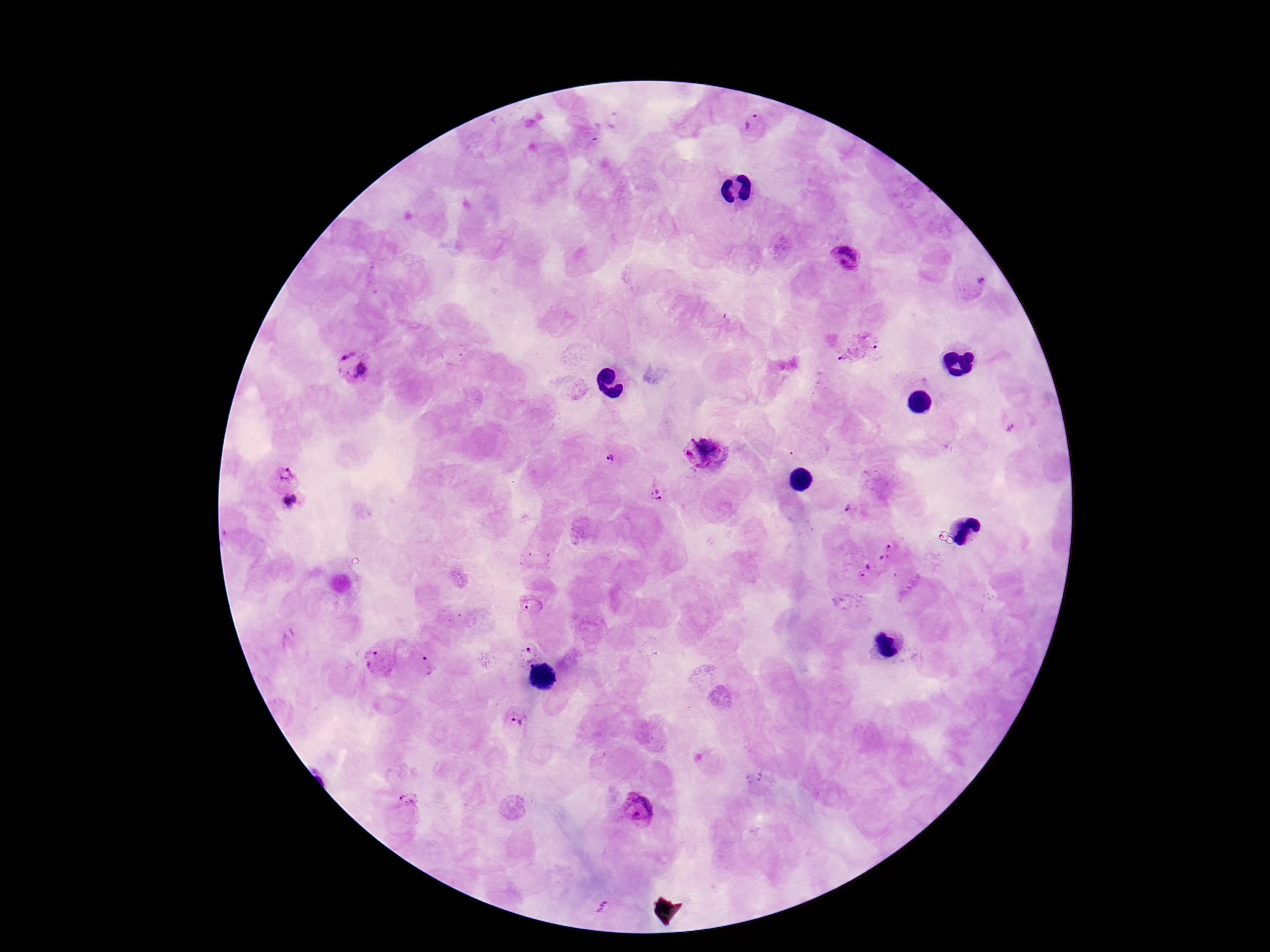
Approximate centers as (x, y) in pixels.
Summary:
  - Plasmodium parasite locations: (753, 127), (849, 260), (860, 345), (349, 365), (1011, 427), (707, 451), (612, 455), (282, 472), (658, 494), (291, 506), (853, 510), (888, 551), (868, 572), (534, 606), (375, 655), (525, 656), (424, 667), (518, 722), (637, 808), (405, 812), (602, 905)
  - Image size: 1270×952 pixels
  - Magnification: 100x
  - Patient malaria status: infected
  - Capture: smartphone camera through the microscope eyepiece
  - Preparation: thick blood smear
  - Stain: Giemsa
  - Field of view: single